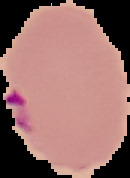 Malaria status: parasitized. Segmented cell region on a black background. Image is 130×178 pixels. From a thin blood smear.